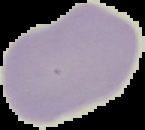
Summary:
  - Result: no Plasmodium parasites seen
  - Image size: 145×130 pixels
  - Image type: segmented cell region on a black background
  - Preparation: thin blood smear